Assess the morphology of the red blood cells.
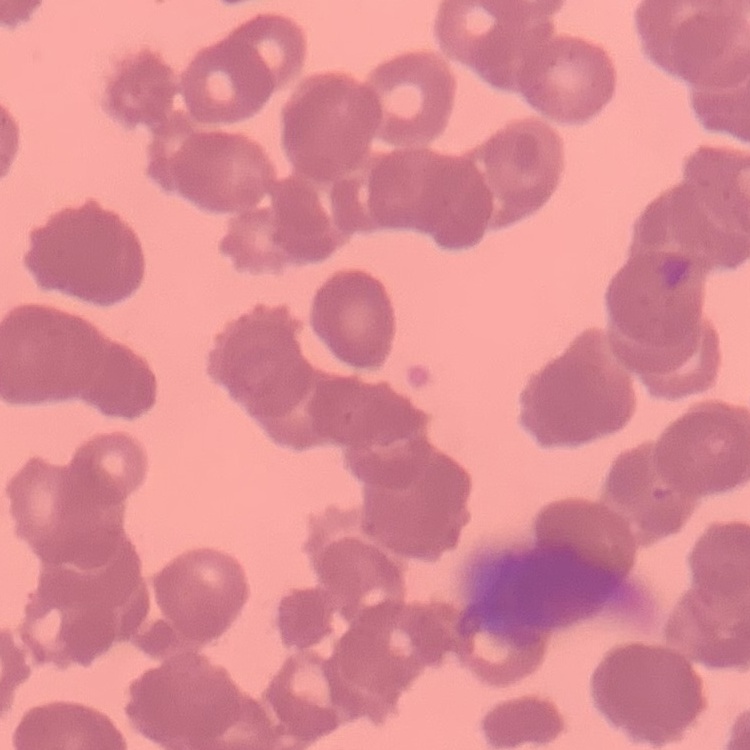
They show rouleaux formation.

Stained with either Field's or Giemsa. One tile cut from a larger photomicrograph. Thin peripheral smear.